Name the cell type shown.
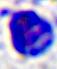

This is a leukocyte.

magnification = 400x
modality = micrograph